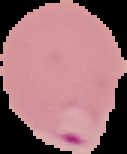

image type = segmented cell region on a black background
preparation = thin blood smear
result = Plasmodium parasites identified
image size = 127×154 pixels